Evaluate for parasitized red blood cells.
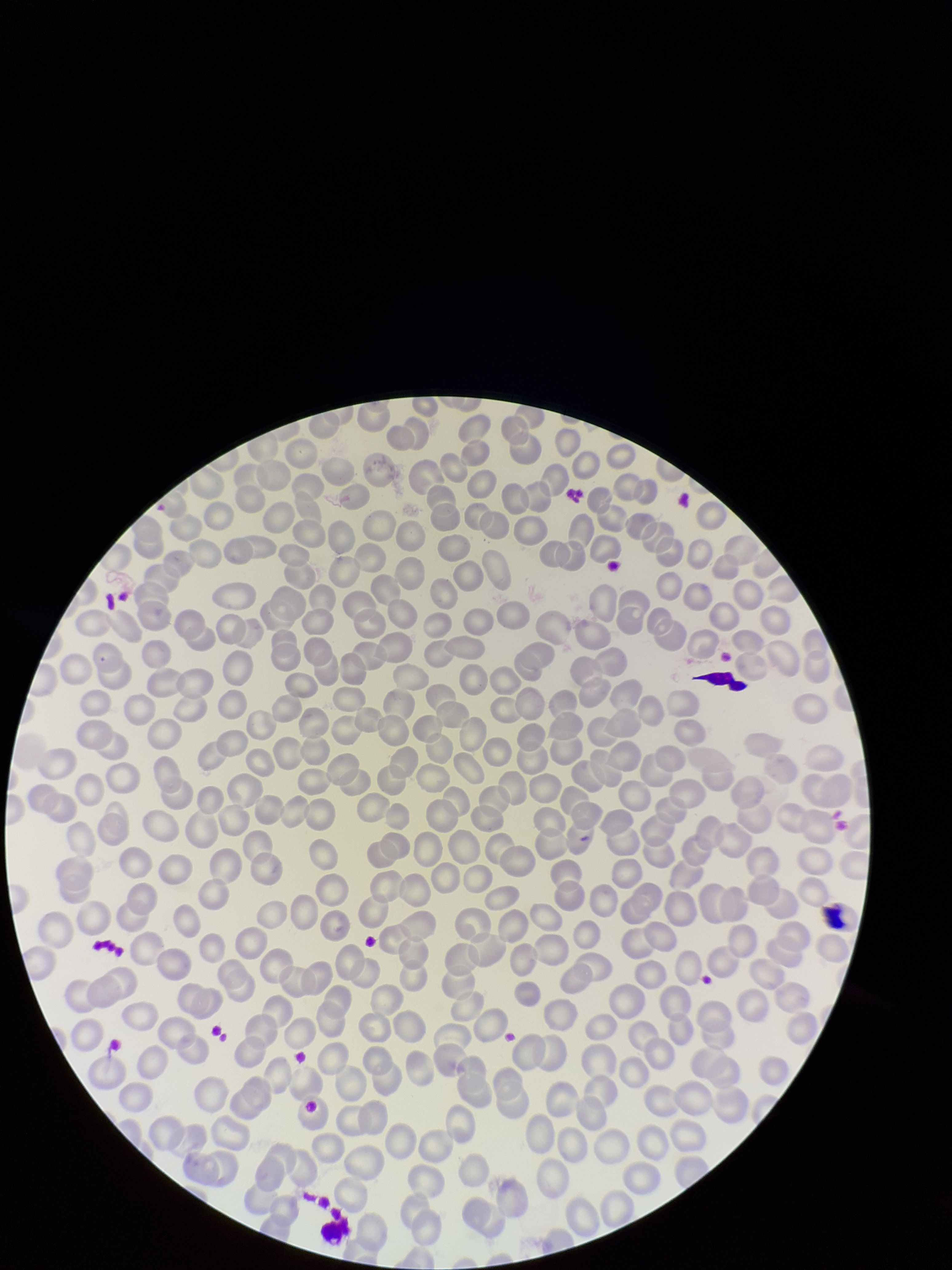
None identified.

Single field of view. Parasitized red blood cell count: 0. Image is 952×1270 pixels. Preparation: thin blood smear. Giemsa stain. Patient malaria status: negative. Smartphone photograph taken through the eyepiece of a microscope. Red blood cell count: 222.